Classify this cell by malaria status.
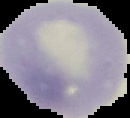

It is uninfected.

{
  "image_type": "cell region segmented out of the field of view; surrounding area masked to black",
  "image_size": "130×118 pixels",
  "preparation": "thin blood smear"
}